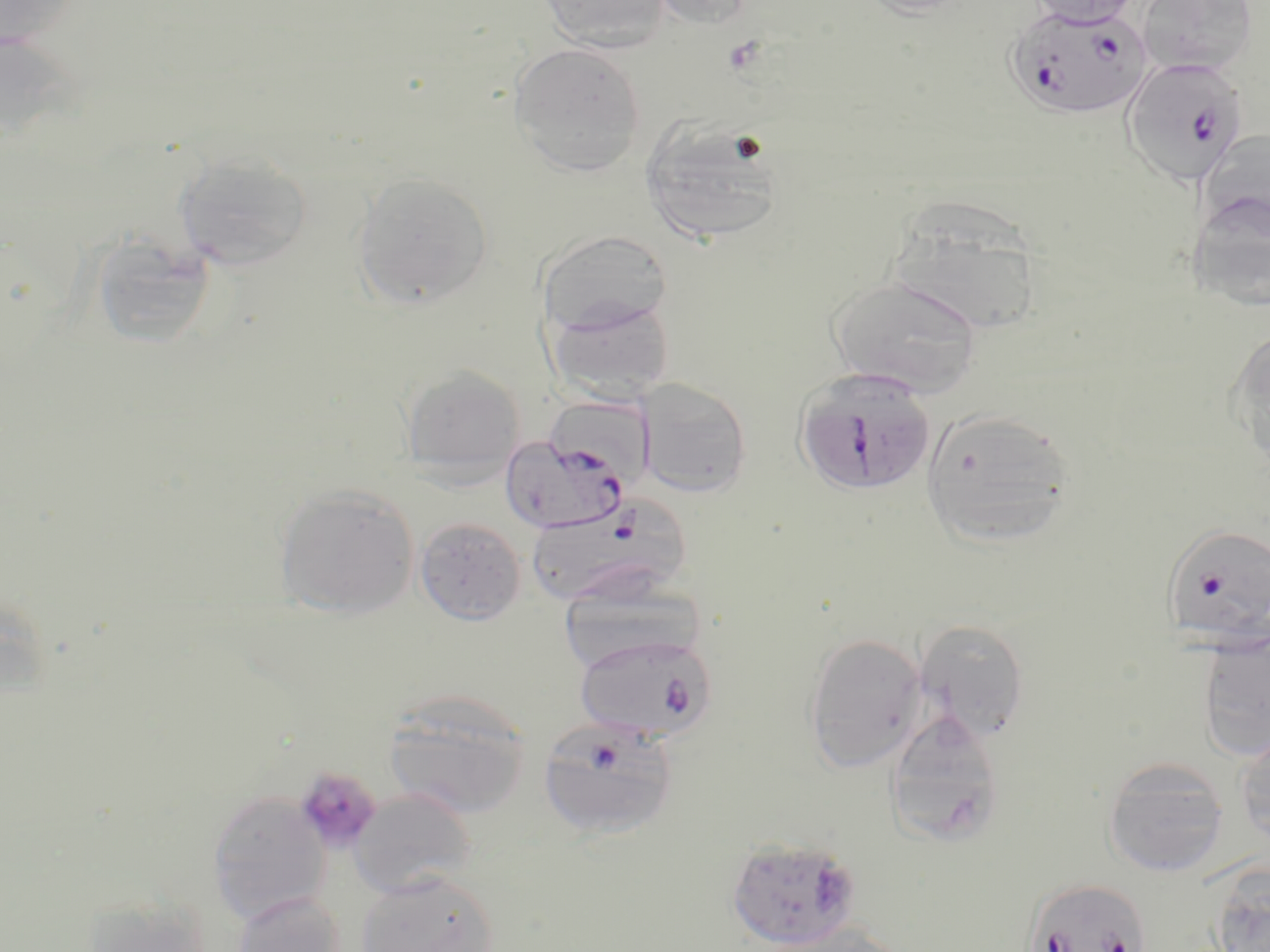

Plasmodium falciparum-infected red blood cell locations = approximate bounding boxes as named x1/y1/x2/y2 corners in pixels: (x1=1006, y1=6, x2=1151, y2=122), (x1=1119, y1=56, x2=1249, y2=187), (x1=793, y1=367, x2=936, y2=497), (x1=499, y1=432, x2=630, y2=534), (x1=523, y1=494, x2=693, y2=611), (x1=1159, y1=523, x2=1270, y2=648), (x1=574, y1=632, x2=718, y2=742), (x1=538, y1=715, x2=679, y2=841), (x1=725, y1=835, x2=862, y2=949), (x1=1020, y1=878, x2=1154, y2=951)
slide-level diagnosis = Plasmodium falciparum
image size = 1270×952 pixels
field of view = single
modality = optical microscopy
stain = May-Grünwald-Giemsa
magnification = 1000x
platelet locations = approximate bounding boxes as named x1/y1/x2/y2 corners in pixels: (x1=294, y1=766, x2=382, y2=852)
uninfected red blood cell locations = approximate bounding boxes as named x1/y1/x2/y2 corners in pixels: (x1=0, y1=0, x2=81, y2=50), (x1=539, y1=0, x2=672, y2=52), (x1=647, y1=0, x2=760, y2=29), (x1=857, y1=0, x2=976, y2=19), (x1=1026, y1=0, x2=1139, y2=27), (x1=1135, y1=0, x2=1258, y2=76), (x1=0, y1=29, x2=82, y2=149), (x1=508, y1=42, x2=646, y2=177), (x1=641, y1=120, x2=784, y2=247), (x1=1199, y1=128, x2=1270, y2=241), (x1=173, y1=151, x2=312, y2=272), (x1=352, y1=172, x2=494, y2=309), (x1=1187, y1=190, x2=1270, y2=313), (x1=887, y1=200, x2=1044, y2=337), (x1=537, y1=229, x2=673, y2=338), (x1=87, y1=233, x2=218, y2=350), (x1=827, y1=274, x2=983, y2=397), (x1=548, y1=298, x2=675, y2=402), (x1=1226, y1=326, x2=1270, y2=472), (x1=400, y1=364, x2=526, y2=484), (x1=636, y1=377, x2=752, y2=497), (x1=921, y1=408, x2=1077, y2=548), (x1=273, y1=483, x2=419, y2=619), (x1=415, y1=517, x2=526, y2=625), (x1=915, y1=619, x2=1031, y2=740), (x1=1198, y1=630, x2=1270, y2=763), (x1=802, y1=631, x2=928, y2=773), (x1=383, y1=689, x2=532, y2=819), (x1=884, y1=710, x2=1005, y2=847), (x1=1235, y1=729, x2=1270, y2=848), (x1=1101, y1=757, x2=1230, y2=878), (x1=350, y1=788, x2=476, y2=896), (x1=207, y1=789, x2=330, y2=923), (x1=1208, y1=866, x2=1270, y2=952), (x1=356, y1=869, x2=499, y2=952), (x1=232, y1=891, x2=346, y2=952), (x1=82, y1=895, x2=215, y2=951), (x1=759, y1=921, x2=907, y2=952)
preparation = thin blood film